Report the malaria status of this cell.
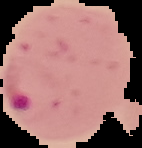
Parasitized.

Cell region segmented out of the field of view; the surrounding area is masked to black. From a thin blood film. Image is 142×148 pixels.